Assess this cell for malaria.
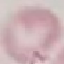
Uninfected.

Giemsa-stained preparation. Thin smear of blood. Photographed with a smartphone camera at the microscope eyepiece. Automatically extracted cell patch, resized to 64 × 64 pixels.